Assess this cell for malaria.
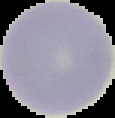

Uninfected.

From a thin blood film. The area outside the segmented cell region is set to black. Image is 115×118 pixels.